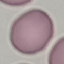
Summary:
  - Result: no malaria parasites detected
  - Capture: smartphone camera at the microscope eyepiece
  - Image type: automatically extracted cell patch, resized to 64 × 64 pixels
  - Preparation: thin blood film
  - Stain: Giemsa